Assess this cell for malaria.
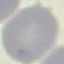

Uninfected.

Thin blood smear. Photographed with a smartphone camera at the microscope eyepiece. Giemsa-stained preparation. Cell patch, automatically extracted from a larger field of view and resized to 64 × 64 pixels.